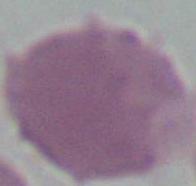 A red blood cell is shown. Photomicrograph. Captured at 1000x magnification.